State which cell type is depicted.
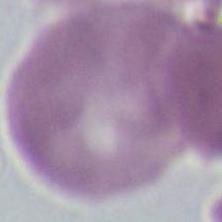

This is an erythrocyte.

modality: micrograph
magnification: 1000x